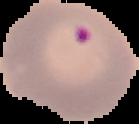

Summary:
  - Result: Plasmodium parasites identified
  - Image size: 139×124 pixels
  - Preparation: thin blood film
  - Image type: segmented cell region with the area outside set to black